State the blood parasite species.
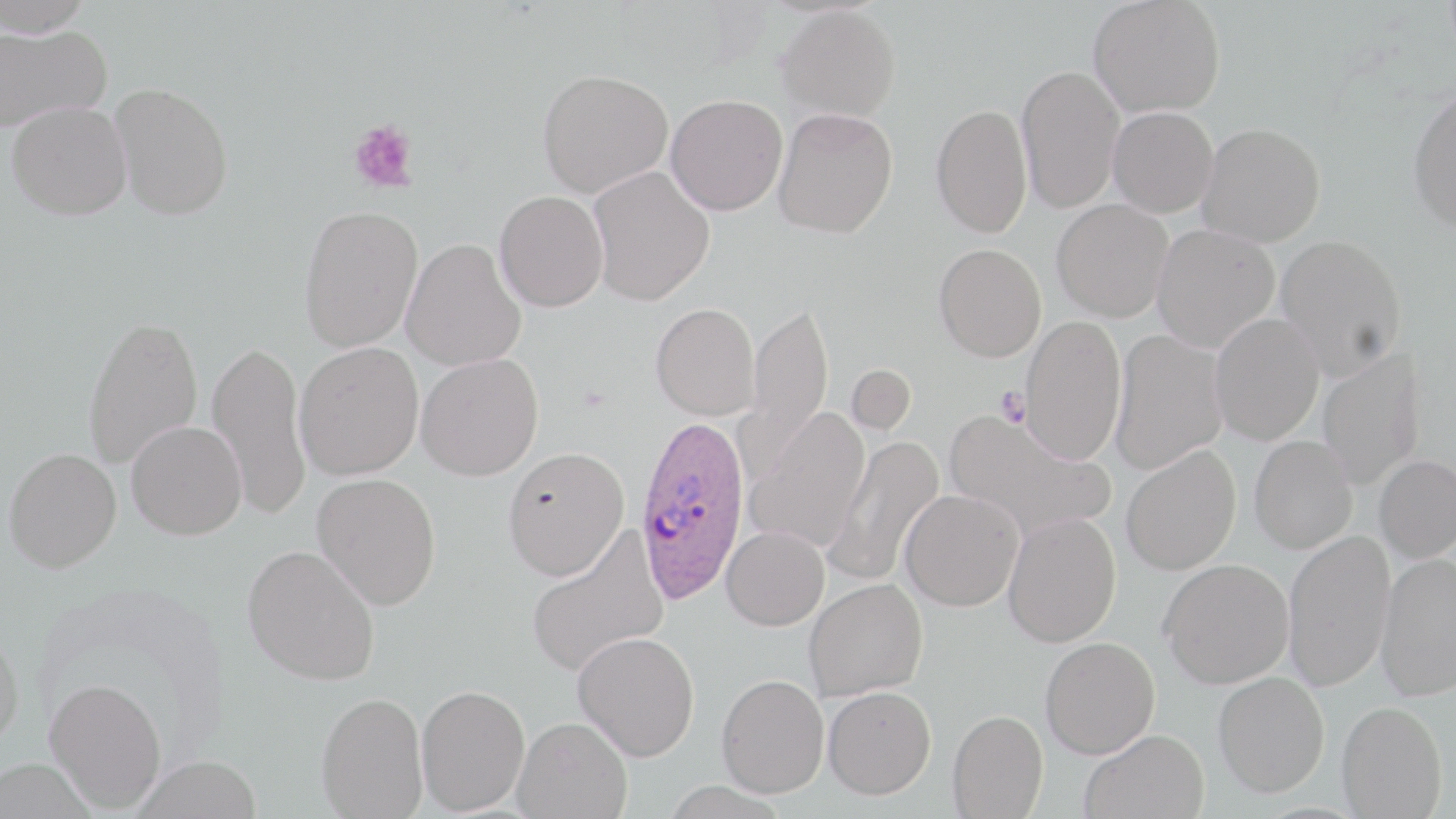

Plasmodium ovale.

Summary:
  - Coordinate format: approximate bounding boxes as (x1,y1)-(x2,y2) corner pairs in pixels
  - Uninfected red blood cell locations: (0,0)-(97,36), (1089,0)-(1227,118), (777,5)-(901,122), (0,23)-(112,132), (1016,64)-(1124,214), (537,67)-(674,197), (110,82)-(234,220), (1408,85)-(1456,234), (665,94)-(788,215), (6,100)-(132,220), (931,103)-(1033,238), (1108,106)-(1219,218), (773,107)-(898,238), (1197,122)-(1326,247), (588,165)-(715,305), (494,190)-(608,312), (1052,199)-(1173,322), (298,203)-(423,353), (1152,224)-(1280,353), (1275,234)-(1407,379), (401,238)-(527,371), (934,243)-(1046,361), (742,299)-(834,477), (650,303)-(759,420), (1211,313)-(1324,445), (82,314)-(203,470), (1019,315)-(1127,465), (1110,329)-(1228,474), (207,338)-(311,521), (293,342)-(424,481), (1317,349)-(1425,491), (415,353)-(543,480), (845,363)-(918,437), (745,407)-(871,553), (946,408)-(1114,541), (126,420)-(247,539), (824,435)-(944,589), (1249,435)-(1358,553), (1121,445)-(1241,575), (503,446)-(629,581), (3,447)-(121,572), (1374,455)-(1456,563), (312,472)-(441,610), (900,490)-(1024,611), (1003,513)-(1121,647), (721,525)-(829,631), (525,527)-(669,677), (1283,529)-(1396,692), (242,544)-(380,685), (1375,552)-(1456,701), (1161,559)-(1294,688), (804,579)-(928,701), (0,626)-(25,749), (573,632)-(699,761), (1041,637)-(1160,758), (1213,672)-(1329,797), (717,674)-(829,798), (44,678)-(167,813), (416,684)-(530,815), (822,686)-(936,799), (316,691)-(427,818), (1336,701)-(1447,818), (947,709)-(1048,818), (513,716)-(632,818), (1080,729)-(1209,819), (132,756)-(261,818), (0,758)-(96,819)
  - Platelet locations: (347,119)-(419,193), (995,386)-(1031,427)
  - Plasmodium ovale-infected red blood cell locations: (634,412)-(750,605)
  - Image size: 1456×819 pixels
  - Field of view: one of a larger specimen
  - Stain: May-Grünwald-Giemsa
  - Magnification: 1000x
  - Modality: light microscopy
  - Preparation: thin blood film